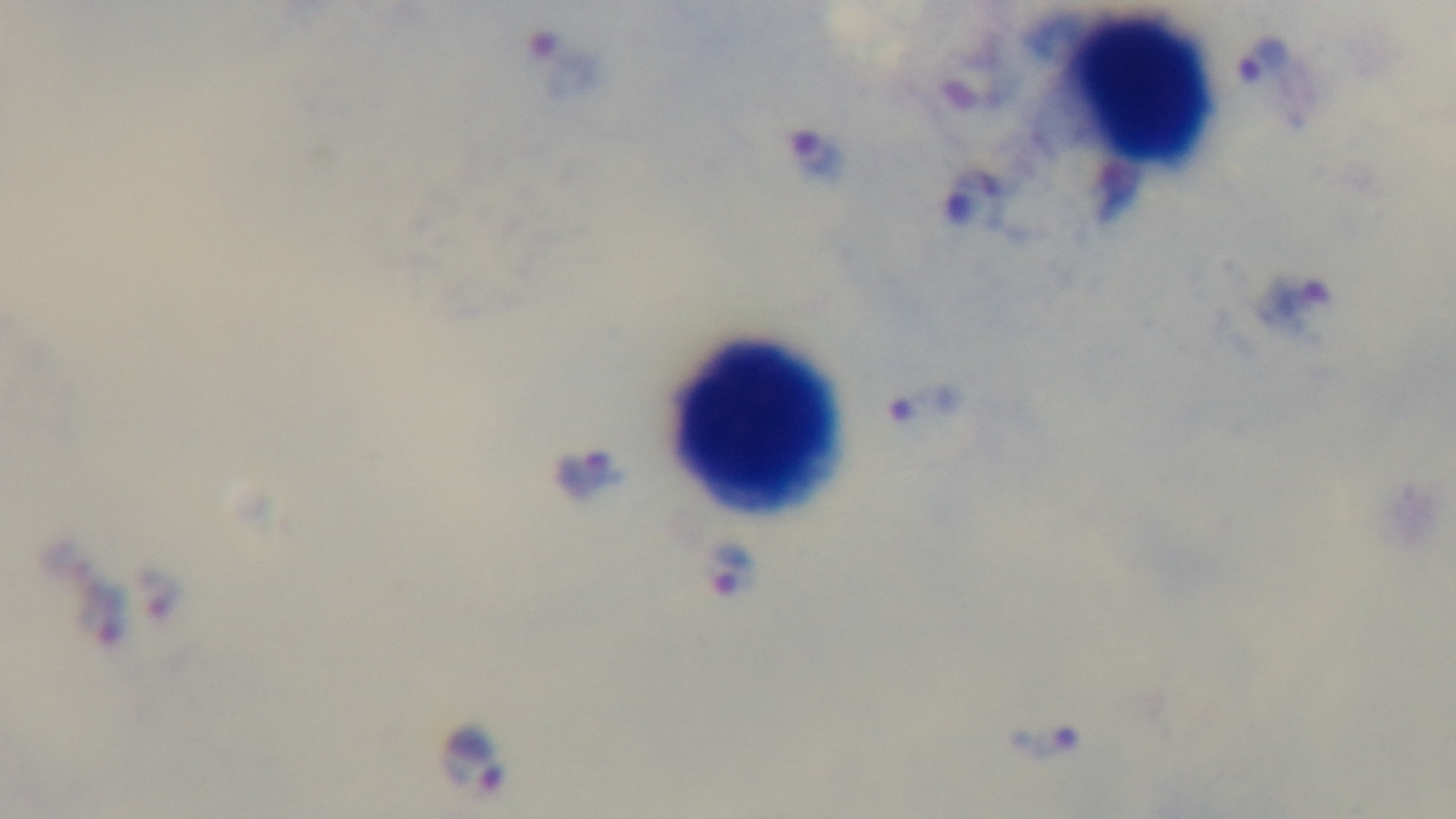
100x oil-immersion objective. Preparation: thick blood film. Malaria status: infected. Giemsa stain. One field from the slide. Light microscopy. Mounted 4K digital camera.